Evaluate for malaria.
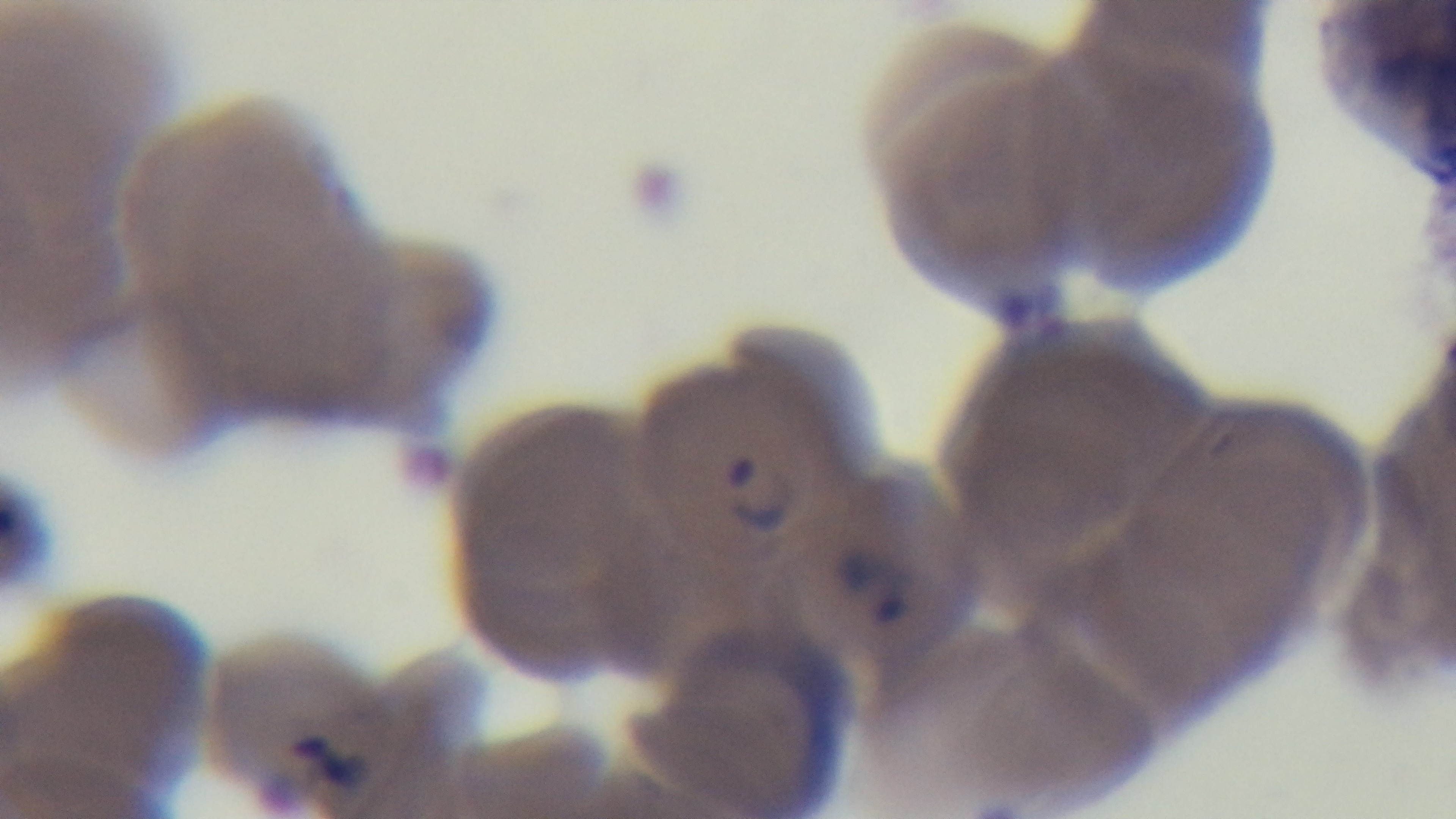
It is infected.

capture: mounted 4K digital camera
modality: light microscopy
objective: 100x oil immersion
stain: Giemsa
preparation: thin blood film
field_of_view: single